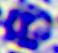

A leukocyte is seen. Captured at 400x magnification. Photomicrograph.